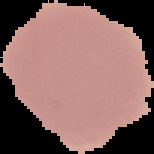

image_size: 154×154 pixels
malaria_status: uninfected
image_type: segmented cell region with the area outside set to black
preparation: thin blood smear